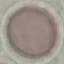

Result: no malaria parasites seen. Automatically extracted cell patch, resized to 64 × 64 pixels. Thin blood smear. Giemsa stain. Photographed with a smartphone camera at the microscope eyepiece.